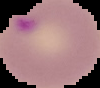
{
  "image_type": "segmented cell region on a black background",
  "image_size": "100×88 pixels",
  "preparation": "thin blood film",
  "result": "Plasmodium parasites identified"
}